Identify the parasite.
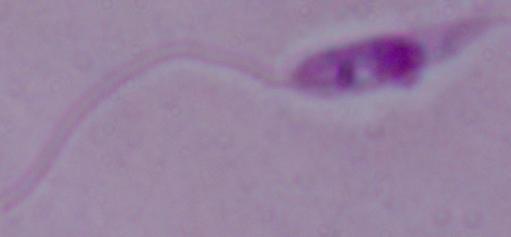
This is Leishmania.

{
  "modality": "photomicrograph",
  "magnification": "1000x"
}